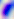
Summary:
  - Magnification: 400x
  - Identification: Toxoplasma gondii
  - Modality: photomicrograph